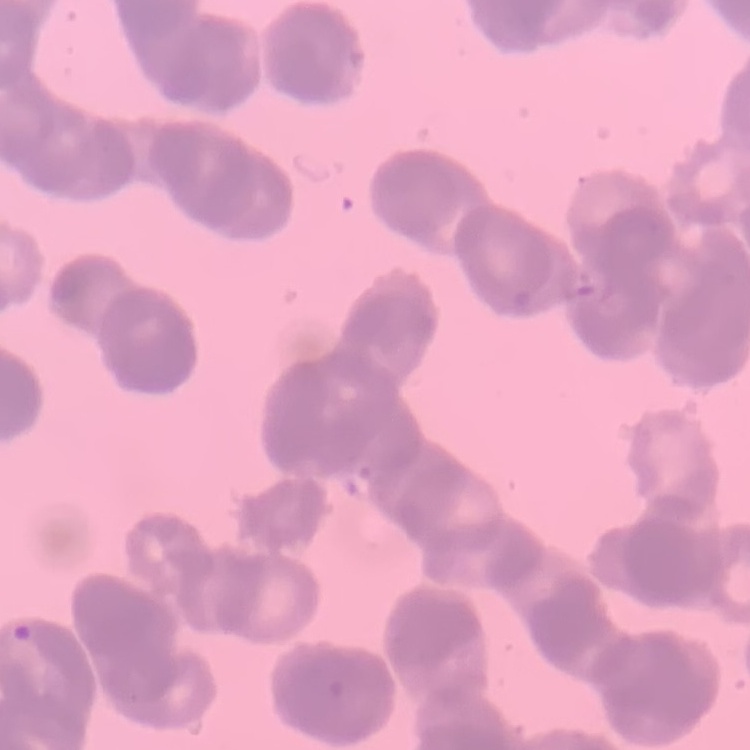
Summary:
  - Red blood cell morphology: rouleaux formation
  - Stain: Field's or Giemsa
  - Preparation: thin peripheral smear
  - Image type: one tile cut from a larger photomicrograph